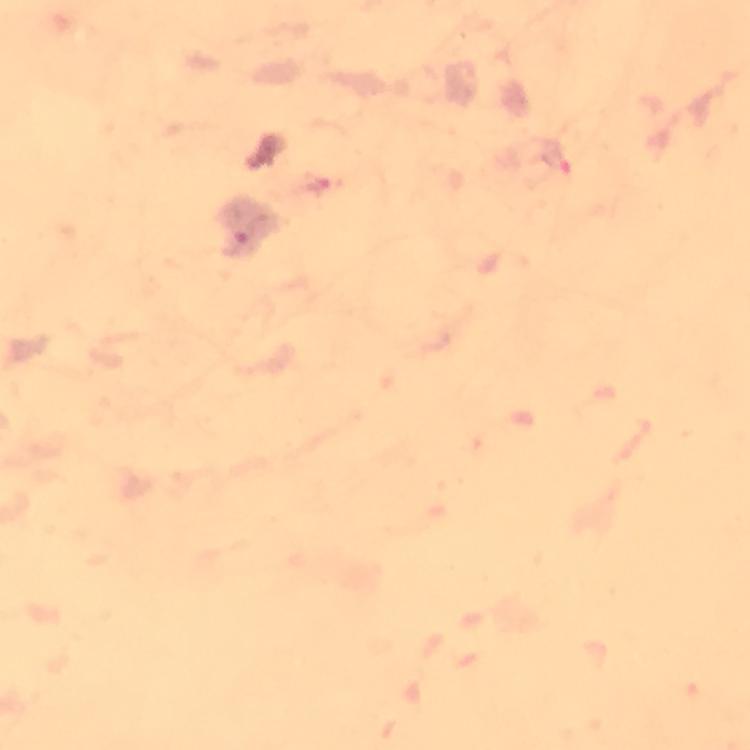
{
  "context": "from a diagnostic examination for malaria",
  "capture": "smartphone mounted on the microscope",
  "plasmodium_parasite_locations": "approximate centers as {x, y} in pixels: {557, 158}",
  "cropped_from": "a single field of view",
  "magnification": "100x",
  "stain": "Giemsa",
  "image_size": "750×750 pixels",
  "immersion_oil": "applied",
  "preparation": "thick blood smear"
}